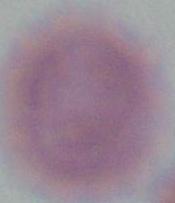
modality = photomicrograph
identification = red blood cell
magnification = 1000x